Report the malaria status of this cell.
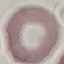

It is uninfected.

Acquired by smartphone through the microscope eyepiece. Giemsa stain. Thin blood film. Automatically extracted cell patch, resized to 64 × 64 pixels.